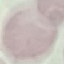
Malaria status: uninfected. Cell patch, automatically extracted from a larger field of view and resized to 64 × 64 pixels. Giemsa stain. Thin smear of blood. Acquired by smartphone through the microscope eyepiece.